Report the malaria status of this cell.
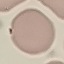

It is uninfected.

Summary:
  - Preparation: thin smear
  - Image type: automatically extracted cell patch, resized to 64 × 64 pixels
  - Capture: smartphone through the microscope eyepiece
  - Stain: Giemsa